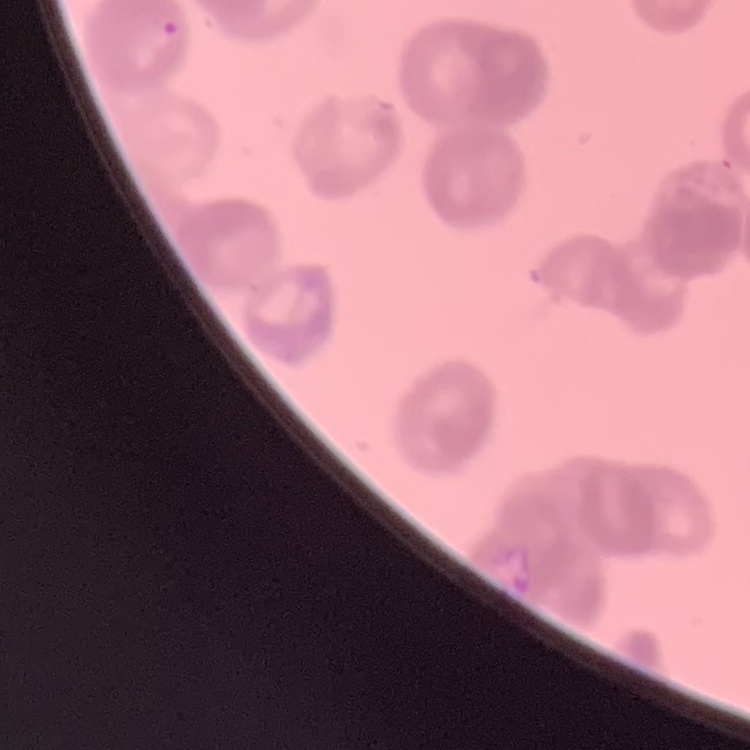
red blood cell morphology = rouleaux formation
image type = one tile cut from a larger photomicrograph
preparation = thin blood film
stain = Field's or Giemsa